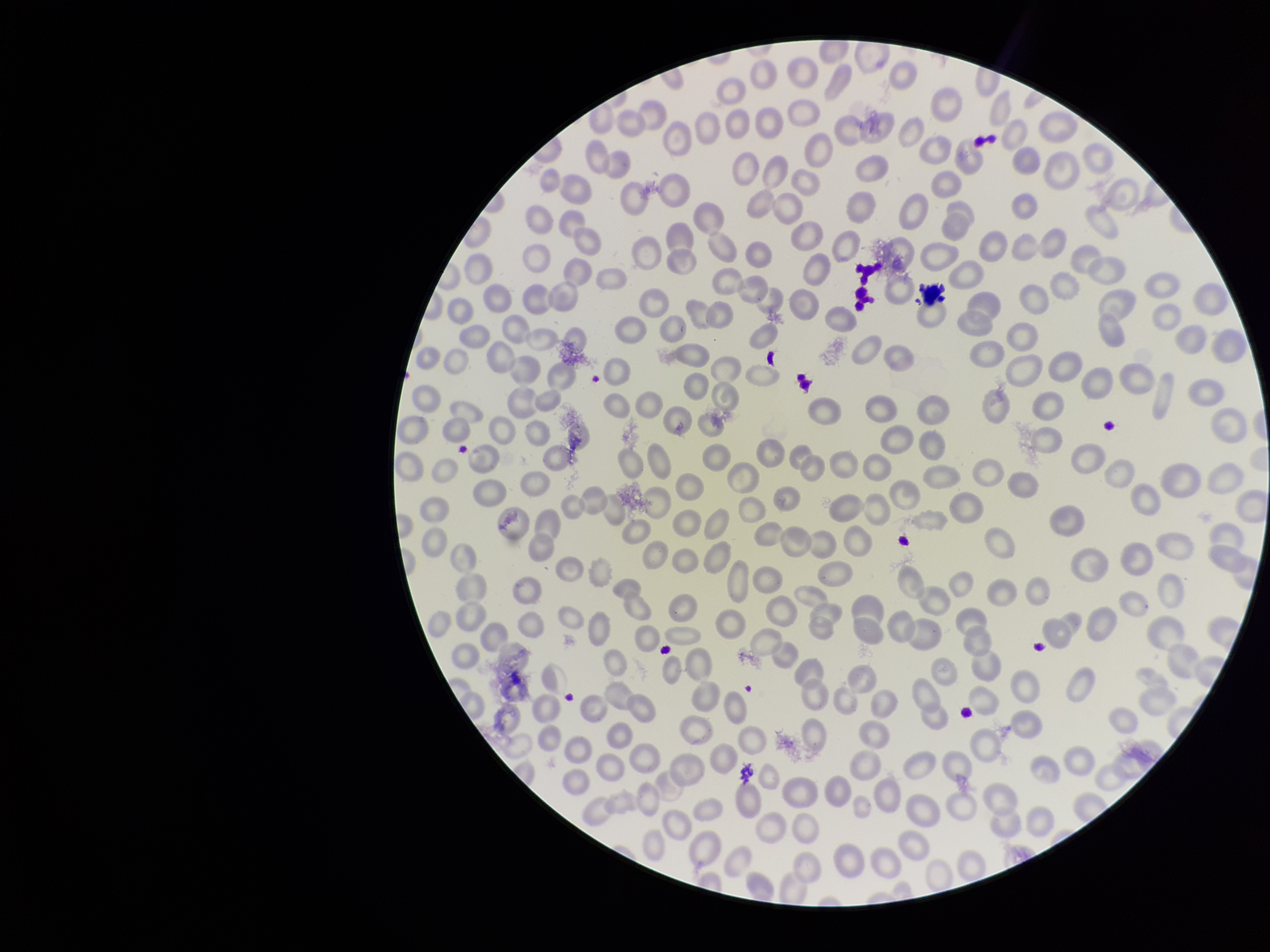
{
  "field_of_view": "one from this slide",
  "parasitized_red_blood_cells": "none identified",
  "image_size": "1270×952 pixels",
  "parasitized_red_blood_cell_count": 0,
  "patient_malaria_status": "negative",
  "capture": "smartphone photograph through the microscope eyepiece",
  "stain": "Giemsa",
  "red_blood_cell_count": 275,
  "preparation": "thin smear"
}